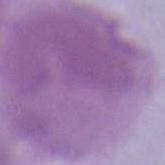

An erythrocyte is shown. Photomicrograph. Captured at 1000x magnification.